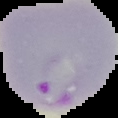
Segmented cell region on a black background. Image is 118×118 pixels. From a thin blood smear. Result: Plasmodium parasites detected.